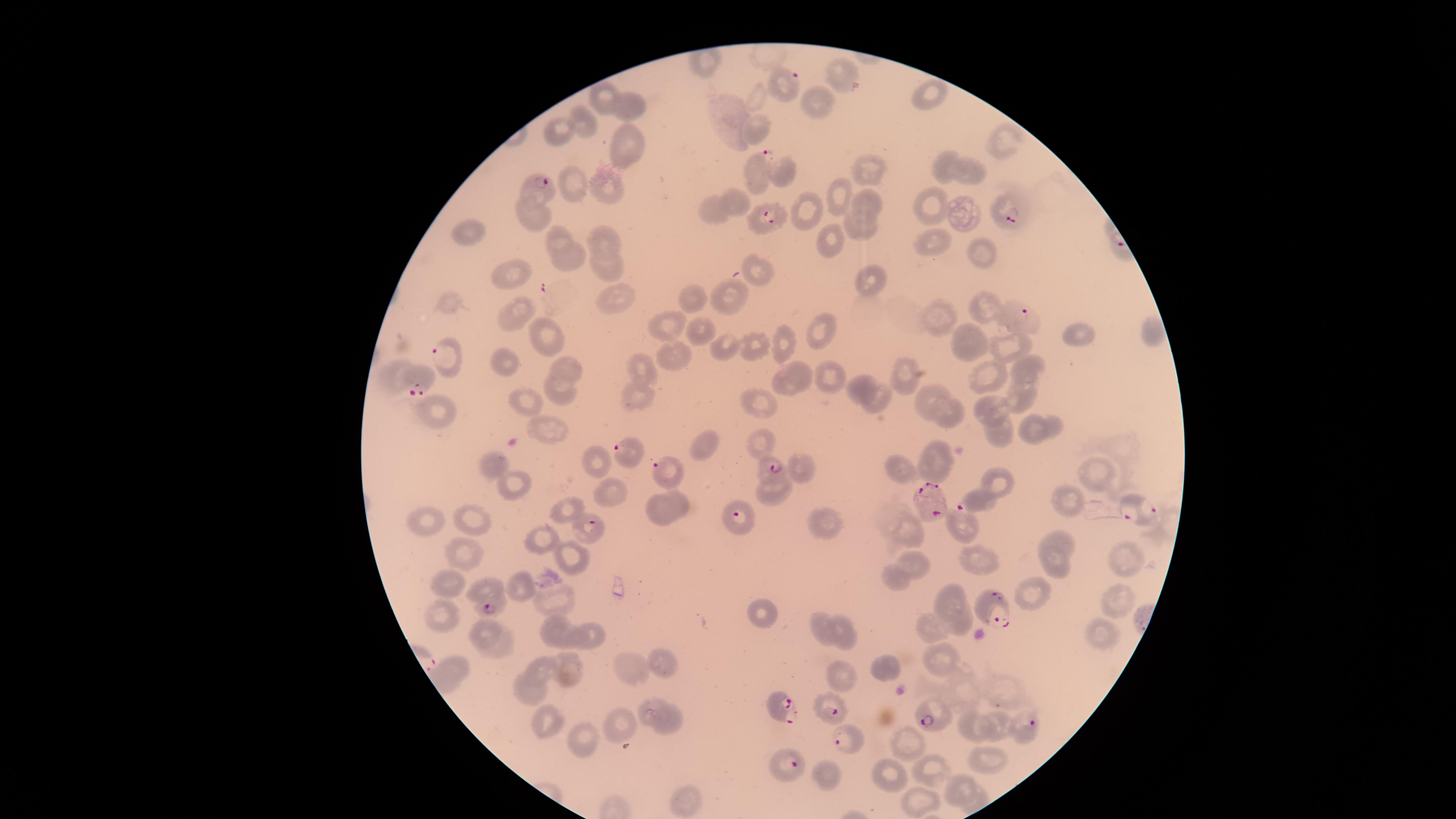
Approximate marker points, in pixels from the top-left corner. Uninfected RBCs: (x=842, y=73), (x=929, y=95), (x=606, y=96), (x=756, y=98), (x=814, y=103), (x=627, y=105), (x=581, y=126), (x=557, y=129), (x=754, y=132), (x=625, y=145), (x=999, y=145), (x=948, y=167), (x=870, y=168), (x=973, y=168), (x=782, y=171), (x=577, y=190), (x=604, y=190), (x=839, y=193), (x=736, y=204), (x=869, y=204), (x=927, y=205), (x=714, y=210), (x=811, y=210), (x=962, y=213), (x=537, y=214), (x=857, y=230), (x=470, y=232), (x=557, y=235), (x=606, y=238), (x=834, y=242), (x=933, y=243), (x=983, y=253), (x=572, y=256), (x=606, y=267), (x=759, y=270), (x=511, y=277), (x=869, y=278), (x=724, y=292), (x=615, y=296), (x=689, y=301), (x=448, y=303), (x=985, y=309), (x=515, y=313), (x=938, y=319), (x=669, y=324), (x=822, y=328), (x=700, y=331), (x=1151, y=337), (x=963, y=338), (x=542, y=339), (x=1078, y=339), (x=783, y=340), (x=759, y=346), (x=1012, y=347), (x=725, y=350), (x=673, y=356), (x=641, y=360), (x=502, y=362), (x=798, y=369), (x=568, y=370), (x=1025, y=371), (x=906, y=372), (x=394, y=375), (x=988, y=377), (x=828, y=378), (x=565, y=388), (x=788, y=388), (x=864, y=388), (x=1021, y=394), (x=642, y=395), (x=925, y=399), (x=882, y=401), (x=767, y=405), (x=533, y=406), (x=1000, y=406), (x=437, y=411), (x=948, y=416), (x=1035, y=426), (x=548, y=432), (x=1002, y=433), (x=760, y=443), (x=707, y=447), (x=933, y=457), (x=591, y=458), (x=495, y=463), (x=804, y=469), (x=901, y=472), (x=1095, y=473), (x=508, y=485), (x=603, y=487), (x=773, y=491), (x=681, y=502), (x=1067, y=502), (x=662, y=509), (x=570, y=511), (x=474, y=517), (x=426, y=519), (x=824, y=522), (x=962, y=524), (x=909, y=533), (x=541, y=539), (x=1059, y=540), (x=1128, y=554), (x=463, y=555), (x=568, y=558), (x=979, y=561), (x=1057, y=564), (x=919, y=567), (x=890, y=583), (x=448, y=585), (x=485, y=587), (x=524, y=587), (x=1030, y=593), (x=1119, y=596), (x=949, y=598), (x=550, y=601), (x=764, y=614), (x=444, y=623), (x=819, y=625), (x=959, y=625), (x=933, y=626), (x=552, y=629), (x=1106, y=633), (x=841, y=634), (x=486, y=635), (x=583, y=639), (x=503, y=649), (x=938, y=658), (x=662, y=662), (x=543, y=667), (x=631, y=667), (x=877, y=667), (x=451, y=668), (x=566, y=673), (x=838, y=675), (x=528, y=690), (x=649, y=708), (x=542, y=719), (x=669, y=724), (x=998, y=726), (x=975, y=728), (x=624, y=729), (x=906, y=741), (x=589, y=742), (x=988, y=759), (x=932, y=771), (x=887, y=775), (x=823, y=777), (x=961, y=790), (x=980, y=795), (x=690, y=802), (x=922, y=803). Parasitized RBCs: (x=789, y=82), (x=757, y=162), (x=544, y=186), (x=1008, y=210), (x=766, y=221), (x=1015, y=308), (x=440, y=354), (x=419, y=382), (x=631, y=452), (x=769, y=466), (x=665, y=471), (x=929, y=500), (x=976, y=500), (x=1133, y=509), (x=738, y=519), (x=588, y=530), (x=492, y=608), (x=992, y=609), (x=779, y=710), (x=831, y=710), (x=931, y=719), (x=1030, y=723), (x=848, y=740), (x=794, y=764). Presence: malaria parasites seen. Thin blood film. Image is 1456×819 pixels. Giemsa stain. Smartphone photograph through the microscope eyepiece. Species: Plasmodium falciparum. Circular visible region. One field of view of the specimen.